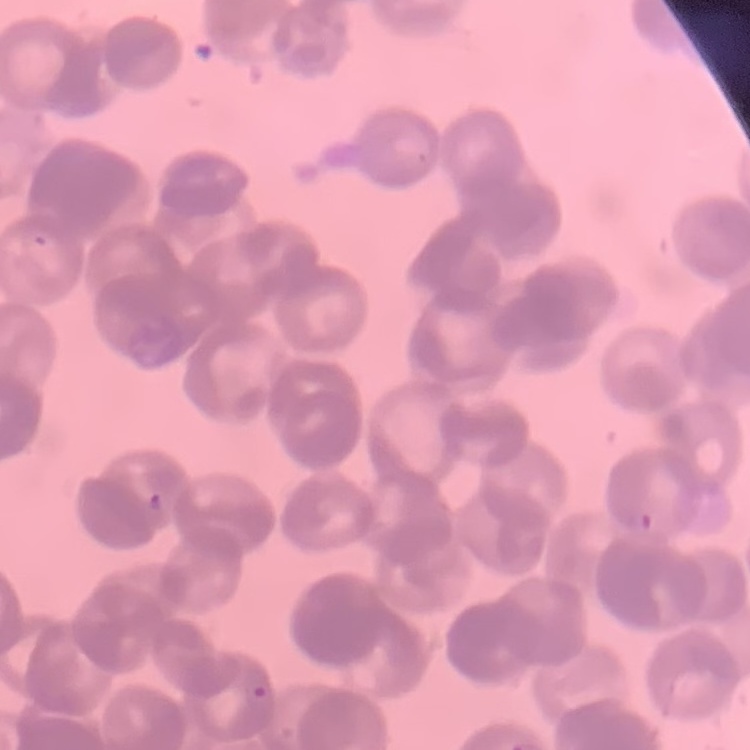
Summary:
  - Red blood cell morphology: rouleaux formation
  - Preparation: thin blood film
  - Stain: Field's or Giemsa
  - Image type: square crop of a larger photomicrograph